Outline each Plasmodium falciparum-infected red blood cell.
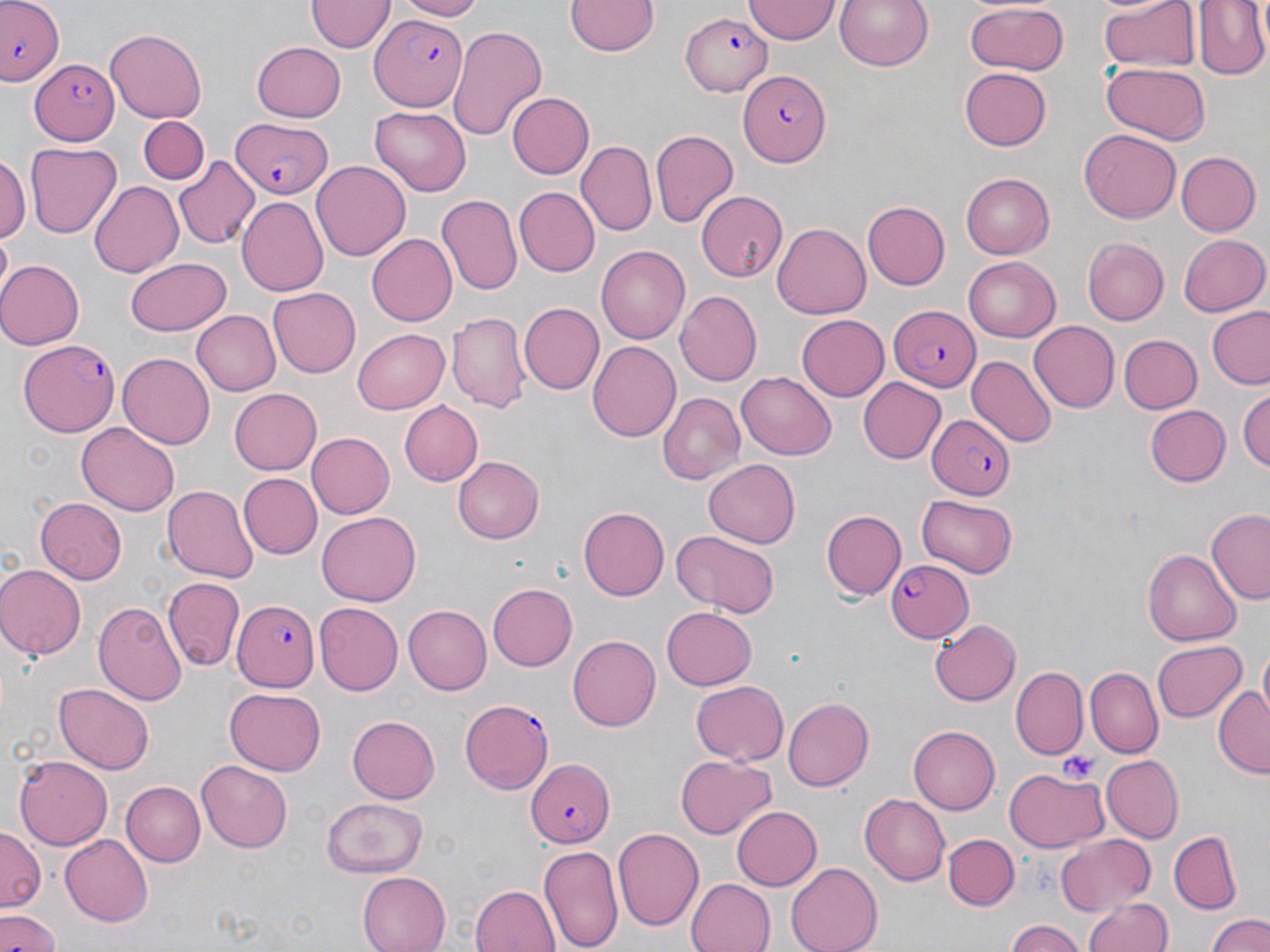
Approximate bounding boxes as (x1,y1)-(x2,y2) corner pairs in pixels.
Plasmodium falciparum-infected red blood cells: (0,1)-(65,87), (680,11)-(771,98), (368,15)-(469,112), (33,54)-(118,147), (740,70)-(830,168), (230,116)-(330,199), (890,304)-(981,391), (18,339)-(120,436), (927,414)-(1016,499), (884,558)-(973,642), (232,600)-(318,692), (458,698)-(555,795), (525,759)-(614,848).

slide-level diagnosis = Plasmodium falciparum
image size = 1270×952 pixels
uninfected red blood cell locations = approximate bounding boxes as (x1,y1)-(x2,y2) corner pairs in pixels: (392,0)-(485,20), (565,0)-(660,58), (742,0)-(841,43), (833,0)-(935,72), (1098,0)-(1200,75), (1194,0)-(1269,80), (304,2)-(393,54), (962,2)-(1069,77), (446,24)-(549,142), (104,29)-(208,122), (129,43)-(210,182), (251,43)-(346,122), (963,59)-(1055,244), (1101,64)-(1209,143), (960,65)-(1051,150), (506,91)-(593,179), (369,107)-(471,195), (136,117)-(207,185), (649,129)-(739,230), (1079,129)-(1182,223), (576,141)-(655,235), (27,143)-(121,237), (1176,152)-(1260,237), (0,156)-(28,241), (172,157)-(259,250), (311,161)-(409,262), (962,171)-(1054,259), (88,180)-(184,279), (515,187)-(600,275), (697,191)-(786,279), (437,193)-(522,296), (237,196)-(330,297), (864,200)-(949,290), (772,224)-(871,318), (366,233)-(460,327), (1175,233)-(1267,317), (1083,237)-(1168,324), (596,244)-(690,346), (961,257)-(1061,343), (124,258)-(230,335), (0,260)-(82,350), (268,288)-(361,376), (675,291)-(763,387), (517,301)-(604,393), (191,309)-(280,396), (1205,309)-(1270,389), (447,310)-(530,412), (798,314)-(890,402), (1027,320)-(1118,410), (354,326)-(449,413), (1120,334)-(1201,414), (589,340)-(683,442), (118,353)-(214,448), (967,355)-(1055,448), (736,372)-(837,460), (858,377)-(947,464), (1237,387)-(1270,475), (229,388)-(321,475), (659,392)-(748,486), (396,400)-(482,487), (1145,405)-(1231,487), (76,422)-(178,518), (306,431)-(395,518), (454,456)-(544,544), (704,460)-(801,547), (237,473)-(321,559), (161,485)-(257,583), (916,495)-(1019,578), (35,498)-(128,583), (579,507)-(669,601), (821,508)-(905,598), (1205,509)-(1270,602), (316,511)-(422,606), (667,528)-(781,618), (1144,547)-(1242,646), (0,564)-(84,661), (162,576)-(243,672), (486,583)-(576,671), (412,592)-(578,684), (93,597)-(188,705), (313,603)-(402,695), (404,604)-(491,694), (661,605)-(756,688), (930,618)-(1020,708), (566,635)-(659,730), (1153,638)-(1245,720), (1012,667)-(1086,757), (1084,668)-(1162,757), (691,682)-(788,764), (55,685)-(154,774), (1212,686)-(1268,777), (224,687)-(326,776), (784,696)-(875,791), (347,715)-(440,804), (908,724)-(1000,816), (13,754)-(112,852), (1100,754)-(1182,843), (675,755)-(775,838), (196,760)-(292,852), (1004,769)-(1106,853), (121,780)-(206,866), (859,794)-(950,884), (321,797)-(425,877), (728,804)-(820,892), (0,827)-(43,916), (613,828)-(703,932), (1169,831)-(1242,913), (944,833)-(1019,911), (1054,834)-(1156,915), (59,835)-(153,926), (538,842)-(624,952), (787,862)-(881,952), (357,871)-(450,952), (685,876)-(775,952), (470,883)-(559,952), (1083,895)-(1175,952), (0,909)-(62,952), (1204,911)-(1270,952), (1003,919)-(1083,952)
magnification = 1000x
field of view = single
preparation = thin blood smear
platelet locations = approximate bounding boxes as (x1,y1)-(x2,y2) corner pairs in pixels: (1059,750)-(1101,784)
stain = May-Grünwald-Giemsa
modality = light microscopy